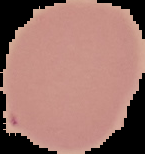
image_type: segmented cell region with the area outside set to black
preparation: thin blood film
malaria_status: uninfected
image_size: 145×154 pixels